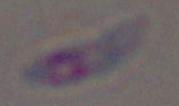

identification: Toxoplasma gondii
magnification: 1000x
modality: micrograph